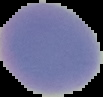

image_size: 103×97 pixels
image_type: segmented cell region on a black background
preparation: thin blood film
result: no malaria parasites seen